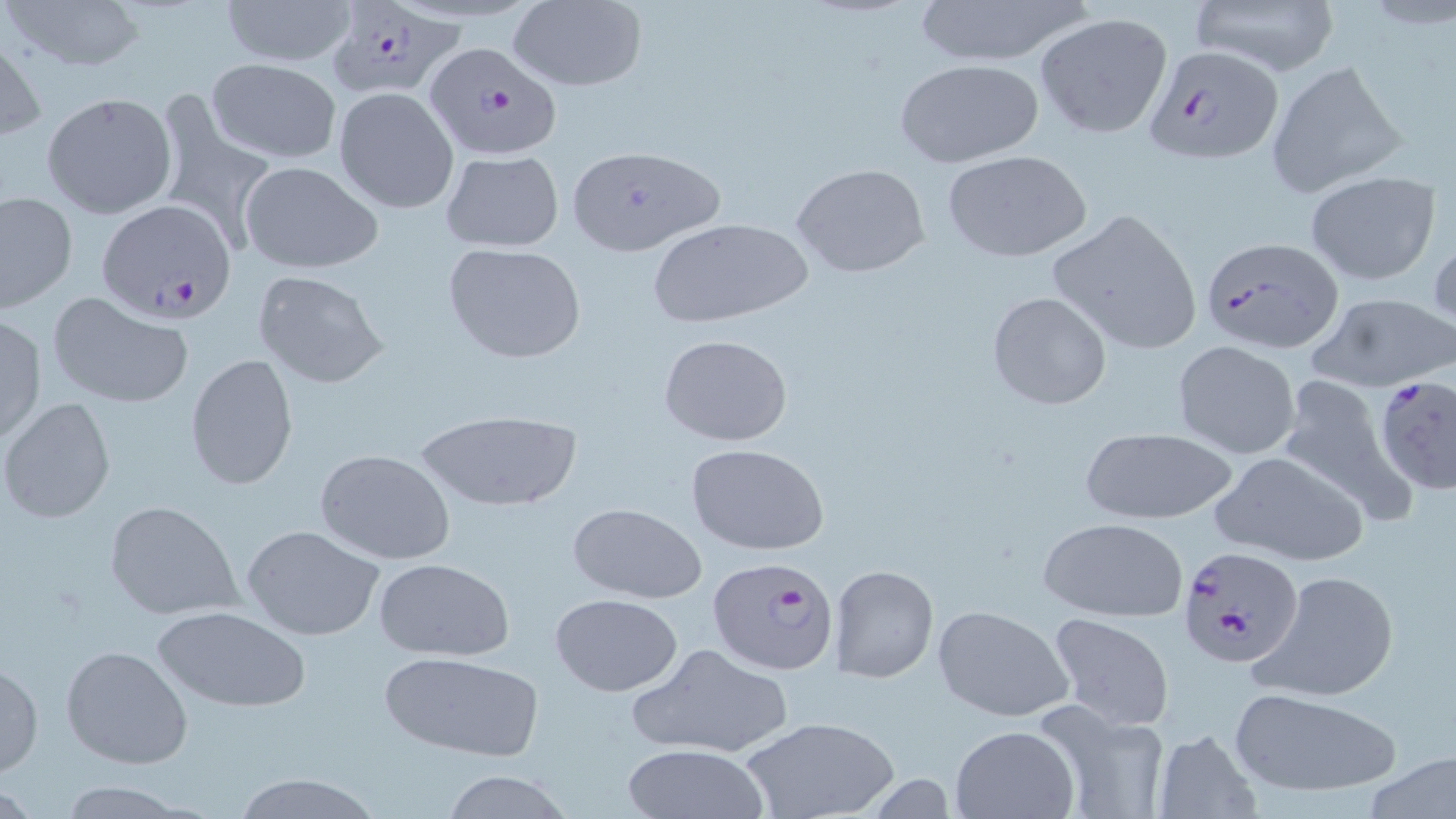
Summary:
  - Coordinate format: approximate bounding boxes as [x1, y1, x2, y2] in pixels
  - Uninfected red blood cell locations: [1, 0, 149, 72], [217, 0, 359, 66], [910, 0, 1095, 67], [1181, 0, 1343, 78], [506, 1, 647, 91], [1033, 13, 1173, 139], [0, 32, 45, 143], [206, 59, 342, 163], [892, 59, 1046, 168], [1264, 60, 1408, 198], [332, 87, 460, 213], [41, 91, 176, 218], [156, 97, 277, 252], [566, 144, 726, 256], [941, 148, 1094, 263], [440, 150, 565, 252], [240, 162, 383, 273], [791, 164, 931, 278], [1305, 171, 1441, 286], [1, 191, 77, 313], [1046, 209, 1204, 355], [648, 215, 814, 328], [1428, 225, 1456, 334], [442, 242, 586, 363], [250, 270, 390, 390], [986, 290, 1111, 411], [1306, 291, 1456, 392], [47, 294, 194, 409], [0, 315, 48, 445], [657, 333, 792, 447], [1172, 340, 1303, 459], [185, 356, 298, 491], [1272, 375, 1412, 518], [1, 398, 116, 524], [414, 409, 583, 513], [1076, 427, 1237, 527], [683, 443, 828, 556], [316, 450, 457, 565], [1211, 451, 1370, 566], [104, 500, 242, 620], [565, 502, 707, 603], [1039, 517, 1189, 622], [242, 525, 386, 641], [371, 557, 517, 662], [828, 564, 938, 683], [1257, 568, 1401, 703], [549, 593, 683, 697], [931, 604, 1075, 722], [152, 605, 311, 712], [1047, 612, 1175, 729], [625, 640, 795, 759], [61, 644, 193, 769], [377, 650, 545, 760], [1, 656, 43, 779], [1228, 686, 1402, 798], [1033, 703, 1172, 819], [741, 716, 899, 819], [949, 725, 1080, 819], [1151, 728, 1265, 817], [621, 742, 771, 819], [1366, 749, 1456, 819], [436, 768, 573, 819], [230, 772, 384, 819], [51, 780, 199, 817]
  - Plasmodium falciparum-infected red blood cell locations: [325, 1, 462, 100], [424, 39, 565, 159], [1145, 45, 1284, 162], [95, 198, 235, 322], [1199, 237, 1343, 354], [1373, 377, 1456, 496], [1177, 544, 1304, 671], [708, 557, 841, 675]
  - Slide-level diagnosis: Plasmodium falciparum
  - Stain: May-Grünwald-Giemsa
  - Preparation: thin blood film
  - Field of view: single
  - Image size: 1456×819 pixels
  - Magnification: 1000x
  - Modality: light microscopy